Assess this cell for malaria.
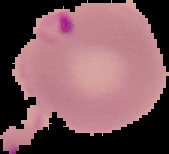
Parasitized.

Image is 169×154 pixels. Cell region segmented out of the field of view; the surrounding area is masked to black. From a thin blood film.